Locate every blood parasite and identify its species.
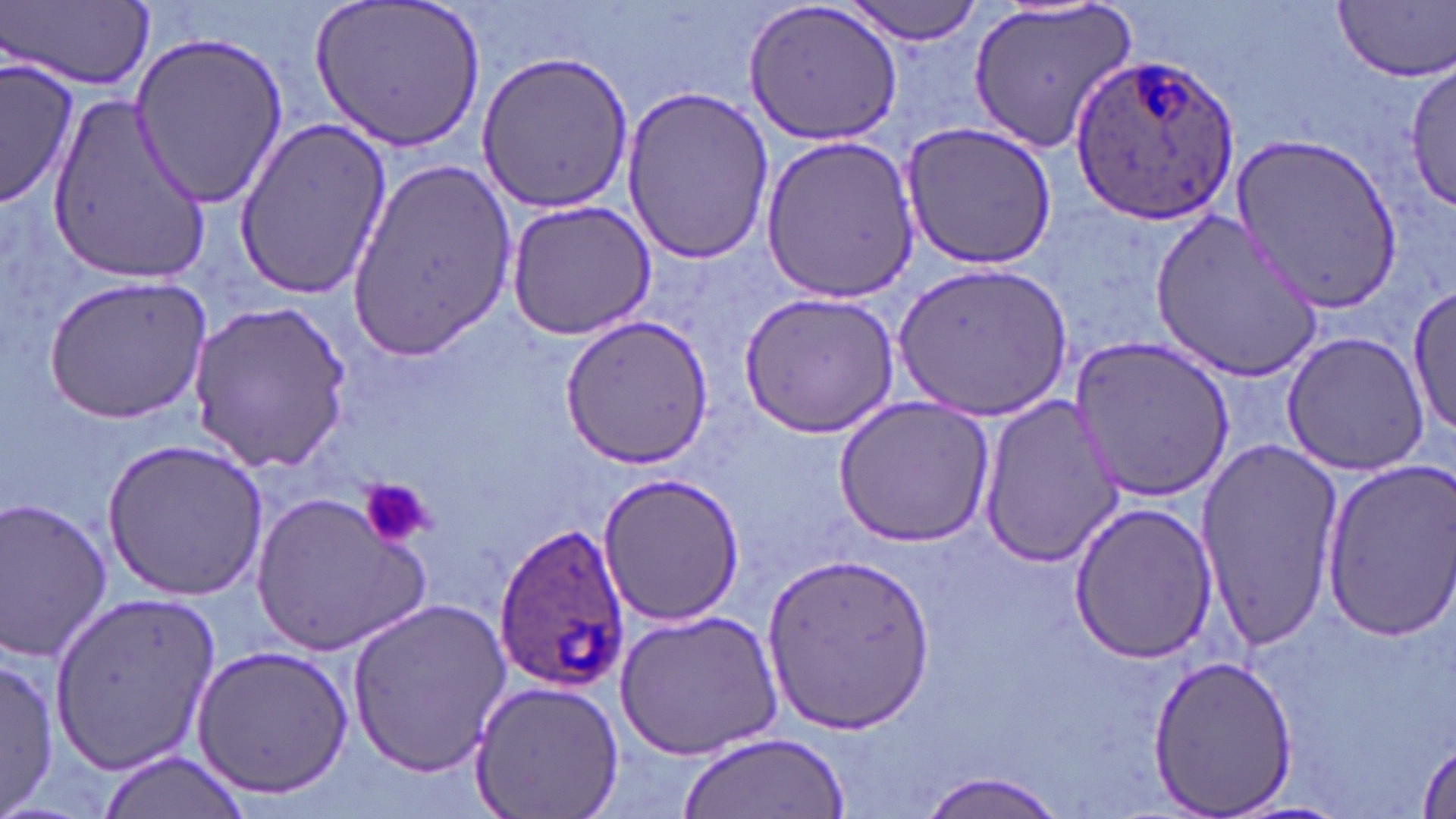
Approximate bounding boxes as named x1/y1/x2/y2 corners in pixels.
Plasmodium ovale-infected red blood cells: (x1=1073, y1=53, x2=1241, y2=226), (x1=490, y1=522, x2=630, y2=693).
No Plasmodium falciparum, Plasmodium malariae, Plasmodium vivax, Babesia divergens, or Trypanosoma brucei observed.

slide_level_diagnosis: Plasmodium ovale
stain: May-Grünwald-Giemsa
modality: light microscopy
preparation: thin blood smear
field_of_view: one of a larger specimen
image_size: 1456×819 pixels
uninfected_red_blood_cell_locations: 'approximate bounding boxes as named x1/y1/x2/y2 corners in pixels: (x1=311, y1=0, x2=489, y2=151), (x1=744, y1=0, x2=906, y2=145), (x1=843, y1=0, x2=986, y2=45), (x1=1333, y1=1, x2=1456, y2=82), (x1=6, y1=2, x2=154, y2=91), (x1=967, y1=2, x2=1137, y2=153), (x1=129, y1=33, x2=288, y2=209), (x1=474, y1=50, x2=635, y2=212), (x1=2, y1=51, x2=80, y2=208), (x1=1405, y1=59, x2=1455, y2=213), (x1=619, y1=85, x2=775, y2=265), (x1=47, y1=91, x2=213, y2=280), (x1=232, y1=119, x2=392, y2=299), (x1=898, y1=120, x2=1056, y2=271), (x1=1233, y1=131, x2=1402, y2=308), (x1=761, y1=133, x2=921, y2=302), (x1=346, y1=160, x2=514, y2=359), (x1=503, y1=201, x2=656, y2=341), (x1=1150, y1=209, x2=1324, y2=380), (x1=893, y1=261, x2=1069, y2=421), (x1=44, y1=276, x2=212, y2=422), (x1=1407, y1=282, x2=1455, y2=441), (x1=740, y1=291, x2=900, y2=435), (x1=189, y1=302, x2=351, y2=471), (x1=559, y1=314, x2=713, y2=468), (x1=1280, y1=329, x2=1431, y2=476), (x1=1069, y1=333, x2=1234, y2=503), (x1=979, y1=395, x2=1126, y2=565), (x1=833, y1=396, x2=994, y2=550), (x1=1193, y1=435, x2=1344, y2=650), (x1=102, y1=436, x2=272, y2=602), (x1=1319, y1=459, x2=1456, y2=640), (x1=597, y1=471, x2=745, y2=628), (x1=251, y1=490, x2=433, y2=656), (x1=0, y1=498, x2=116, y2=663), (x1=1067, y1=501, x2=1216, y2=663), (x1=759, y1=554, x2=936, y2=733), (x1=47, y1=595, x2=222, y2=772), (x1=344, y1=597, x2=513, y2=776), (x1=615, y1=610, x2=782, y2=762), (x1=189, y1=644, x2=354, y2=802), (x1=1145, y1=653, x2=1298, y2=819), (x1=0, y1=656, x2=58, y2=812), (x1=465, y1=678, x2=625, y2=819), (x1=679, y1=731, x2=850, y2=819), (x1=1414, y1=741, x2=1456, y2=818), (x1=94, y1=750, x2=251, y2=819), (x1=916, y1=771, x2=1070, y2=818)'
platelet_locations: 'approximate bounding boxes as named x1/y1/x2/y2 corners in pixels: (x1=360, y1=478, x2=432, y2=552)'
magnification: 1000x